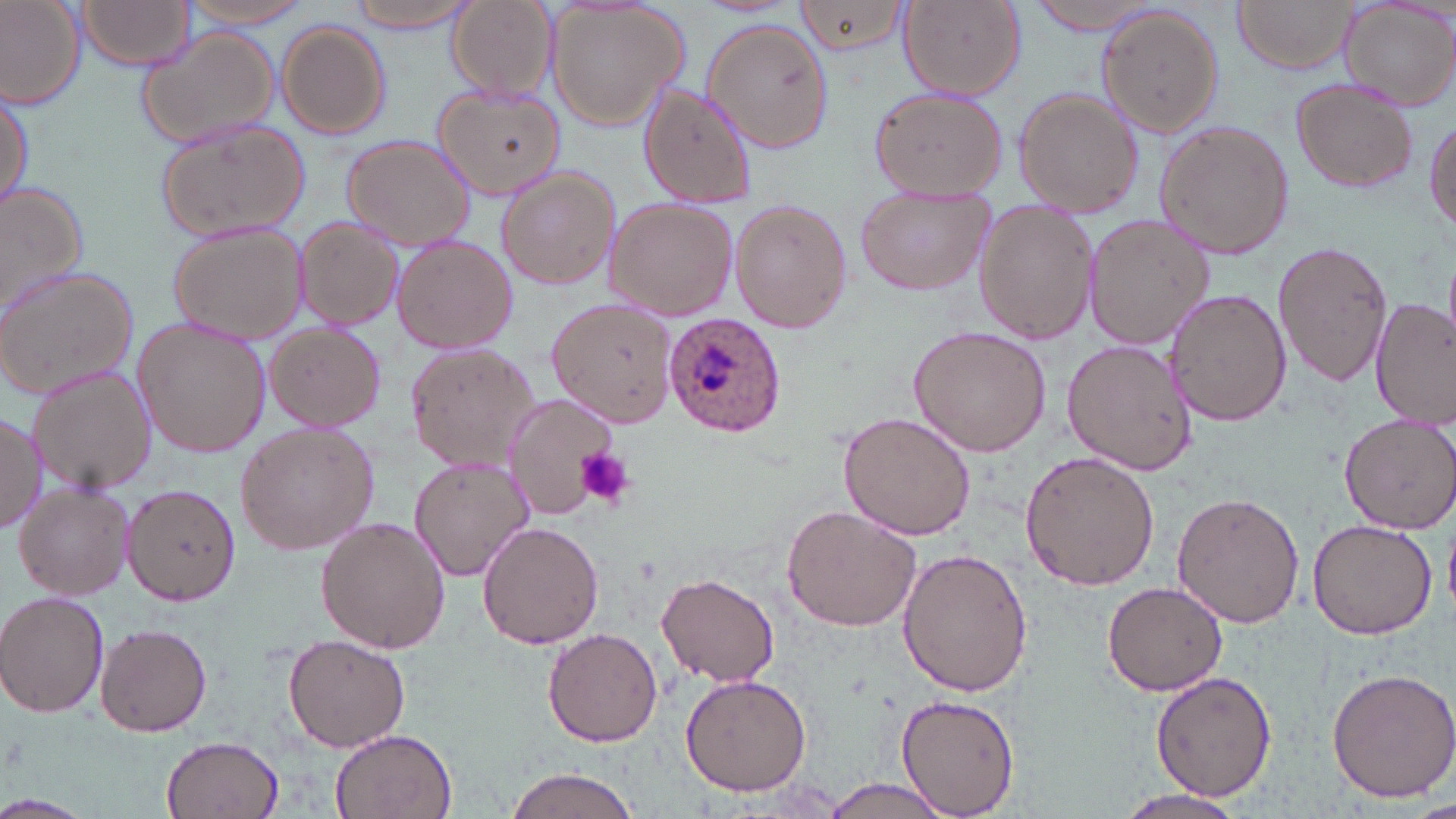
slide-level diagnosis = Plasmodium ovale
modality = optical microscopy
Plasmodium ovale-infected red blood cell locations = approximate bounding boxes as named x1/y1/x2/y2 corners in pixels: (x1=661, y1=316, x2=785, y2=437)
image size = 1456×819 pixels
platelet locations = approximate bounding boxes as named x1/y1/x2/y2 corners in pixels: (x1=576, y1=446, x2=634, y2=508)
field of view = single
stain = May-Grünwald-Giemsa
uninfected red blood cell locations = approximate bounding boxes as named x1/y1/x2/y2 corners in pixels: (x1=73, y1=0, x2=198, y2=71), (x1=174, y1=0, x2=319, y2=31), (x1=350, y1=0, x2=475, y2=33), (x1=1231, y1=0, x2=1359, y2=74), (x1=0, y1=1, x2=87, y2=107), (x1=791, y1=1, x2=913, y2=54), (x1=1028, y1=1, x2=1169, y2=34), (x1=1339, y1=1, x2=1456, y2=110), (x1=447, y1=2, x2=556, y2=103), (x1=897, y1=2, x2=1024, y2=100), (x1=541, y1=3, x2=689, y2=134), (x1=1096, y1=6, x2=1224, y2=136), (x1=702, y1=18, x2=837, y2=155), (x1=277, y1=21, x2=391, y2=139), (x1=136, y1=27, x2=283, y2=149), (x1=1292, y1=76, x2=1421, y2=194), (x1=432, y1=82, x2=566, y2=202), (x1=637, y1=83, x2=756, y2=210), (x1=868, y1=86, x2=1010, y2=201), (x1=1, y1=88, x2=32, y2=213), (x1=1013, y1=88, x2=1144, y2=216), (x1=1426, y1=111, x2=1456, y2=238), (x1=153, y1=117, x2=310, y2=245), (x1=1156, y1=120, x2=1294, y2=260), (x1=340, y1=135, x2=479, y2=250), (x1=496, y1=165, x2=623, y2=289), (x1=0, y1=180, x2=91, y2=316), (x1=854, y1=188, x2=993, y2=298), (x1=604, y1=198, x2=738, y2=320), (x1=730, y1=200, x2=852, y2=333), (x1=971, y1=204, x2=1100, y2=345), (x1=1084, y1=214, x2=1216, y2=351), (x1=293, y1=220, x2=405, y2=331), (x1=168, y1=223, x2=307, y2=342), (x1=390, y1=233, x2=516, y2=354), (x1=1273, y1=240, x2=1393, y2=387), (x1=0, y1=264, x2=140, y2=397), (x1=1166, y1=288, x2=1290, y2=427), (x1=549, y1=296, x2=678, y2=427), (x1=1371, y1=299, x2=1455, y2=430), (x1=132, y1=314, x2=271, y2=460), (x1=263, y1=322, x2=386, y2=431), (x1=908, y1=326, x2=1052, y2=458), (x1=1060, y1=339, x2=1196, y2=475), (x1=407, y1=343, x2=543, y2=473), (x1=26, y1=362, x2=156, y2=497), (x1=502, y1=394, x2=620, y2=519), (x1=0, y1=410, x2=46, y2=534), (x1=838, y1=412, x2=975, y2=541), (x1=1339, y1=412, x2=1455, y2=535), (x1=234, y1=421, x2=379, y2=557), (x1=1019, y1=450, x2=1160, y2=591), (x1=408, y1=456, x2=533, y2=582), (x1=126, y1=483, x2=242, y2=606), (x1=14, y1=484, x2=135, y2=601), (x1=1173, y1=491, x2=1307, y2=627), (x1=781, y1=504, x2=921, y2=633), (x1=316, y1=516, x2=450, y2=654), (x1=1308, y1=518, x2=1440, y2=640), (x1=476, y1=521, x2=604, y2=649), (x1=899, y1=547, x2=1033, y2=698), (x1=657, y1=572, x2=781, y2=688), (x1=1103, y1=580, x2=1229, y2=697), (x1=0, y1=591, x2=110, y2=718), (x1=95, y1=620, x2=212, y2=737), (x1=543, y1=627, x2=664, y2=747), (x1=285, y1=634, x2=411, y2=753), (x1=1326, y1=665, x2=1456, y2=800), (x1=1151, y1=671, x2=1277, y2=802), (x1=681, y1=675, x2=811, y2=795), (x1=894, y1=694, x2=1020, y2=819), (x1=326, y1=725, x2=459, y2=818), (x1=160, y1=736, x2=284, y2=819), (x1=499, y1=768, x2=645, y2=819), (x1=820, y1=779, x2=957, y2=818), (x1=1109, y1=790, x2=1252, y2=819), (x1=0, y1=796, x2=92, y2=818)
preparation = thin blood smear
magnification = 1000x